Report the malaria status of this cell.
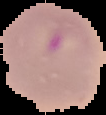
Parasitized.

preparation = thin blood film
image type = segmented cell region with the area outside set to black
image size = 106×115 pixels